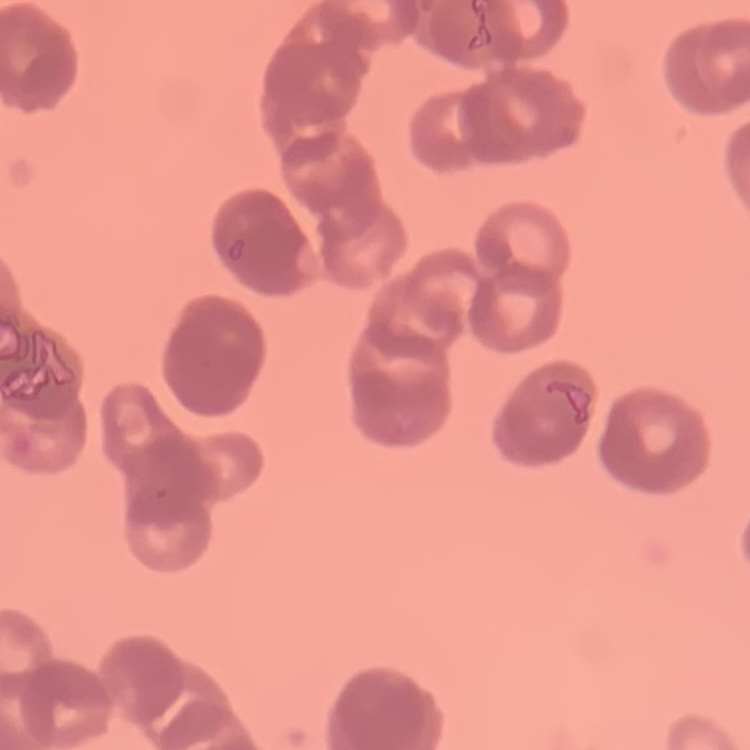
Summary:
  - Red blood cell morphology: rouleaux formation
  - Preparation: thin peripheral smear
  - Image type: one tile cut from a larger photomicrograph
  - Stain: Field's or Giemsa